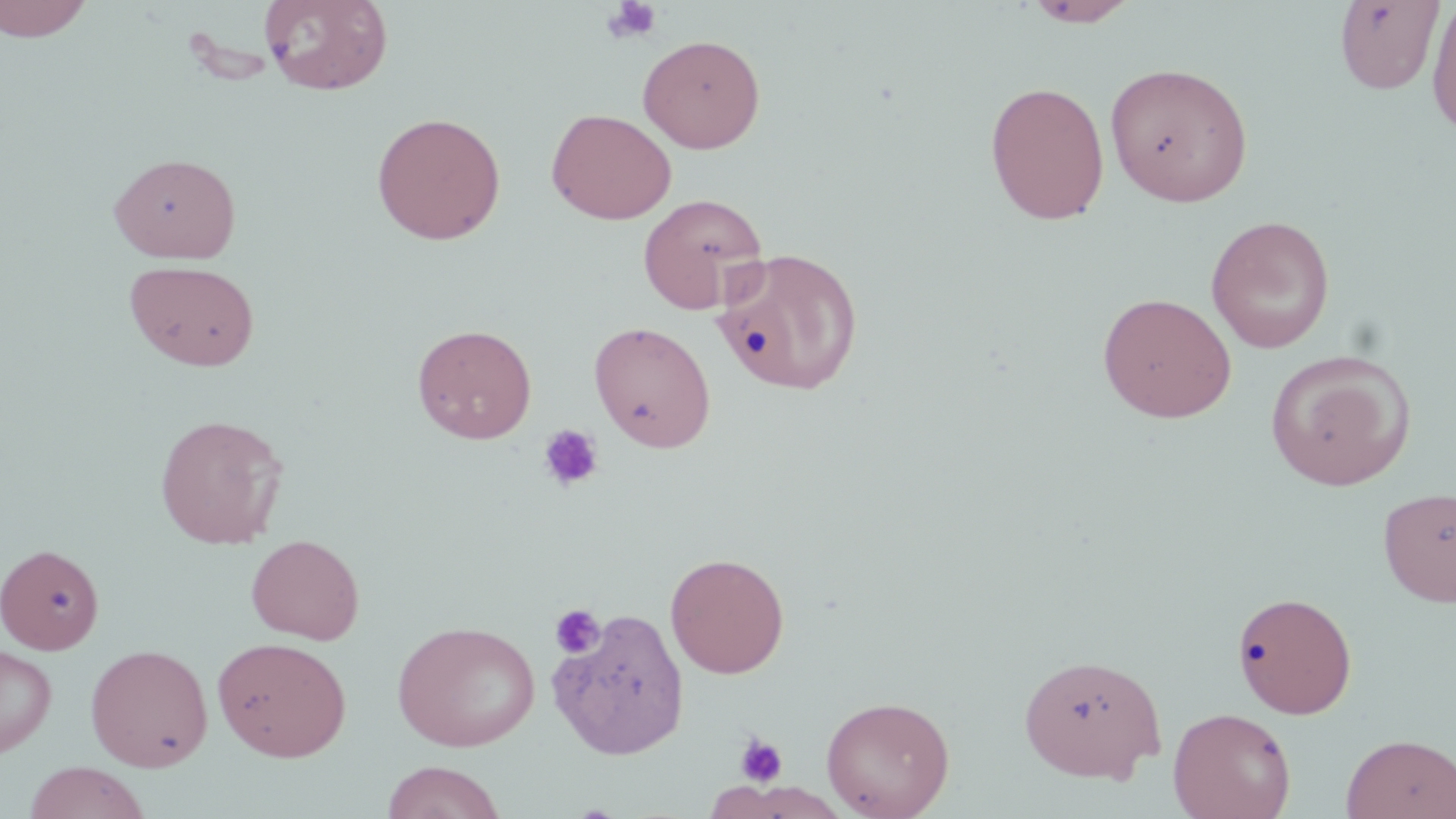
slide_level_diagnosis: no evidence of blood parasites
stain: May-Grünwald-Giemsa
image_size: 1456×819 pixels
preparation: thin blood smear
magnification: 1000x
field_of_view: one of a larger specimen
uninfected_red_blood_cell_locations: 'approximate bounding boxes as named x1/y1/x2/y2 corners in pixels: (x1=0, y1=0, x2=95, y2=42), (x1=260, y1=0, x2=394, y2=96), (x1=1426, y1=0, x2=1456, y2=140), (x1=1024, y1=1, x2=1140, y2=27), (x1=1333, y1=1, x2=1445, y2=95), (x1=638, y1=34, x2=766, y2=153), (x1=1105, y1=62, x2=1254, y2=207), (x1=985, y1=80, x2=1110, y2=226), (x1=546, y1=108, x2=676, y2=225), (x1=370, y1=111, x2=507, y2=245), (x1=109, y1=152, x2=241, y2=263), (x1=638, y1=193, x2=769, y2=314), (x1=1205, y1=215, x2=1336, y2=354), (x1=713, y1=246, x2=863, y2=397), (x1=124, y1=259, x2=260, y2=372), (x1=1097, y1=292, x2=1237, y2=423), (x1=588, y1=320, x2=716, y2=453), (x1=412, y1=323, x2=537, y2=444), (x1=1266, y1=350, x2=1416, y2=491), (x1=153, y1=412, x2=288, y2=549), (x1=1378, y1=486, x2=1456, y2=608), (x1=246, y1=533, x2=365, y2=645), (x1=0, y1=543, x2=104, y2=654), (x1=665, y1=551, x2=789, y2=678), (x1=1233, y1=590, x2=1358, y2=718), (x1=548, y1=607, x2=690, y2=760), (x1=392, y1=620, x2=541, y2=752), (x1=212, y1=636, x2=352, y2=761), (x1=84, y1=643, x2=214, y2=772), (x1=0, y1=644, x2=57, y2=757), (x1=1018, y1=653, x2=1166, y2=782), (x1=820, y1=695, x2=955, y2=818), (x1=1167, y1=706, x2=1297, y2=819), (x1=1341, y1=733, x2=1456, y2=819), (x1=380, y1=760, x2=508, y2=819), (x1=23, y1=761, x2=151, y2=819)'
modality: optical microscopy
platelet_locations: 'approximate bounding boxes as named x1/y1/x2/y2 corners in pixels: (x1=601, y1=0, x2=664, y2=44), (x1=537, y1=424, x2=604, y2=493), (x1=549, y1=603, x2=606, y2=659), (x1=734, y1=733, x2=788, y2=788)'